Give a bounding box for every leukocyte visible.
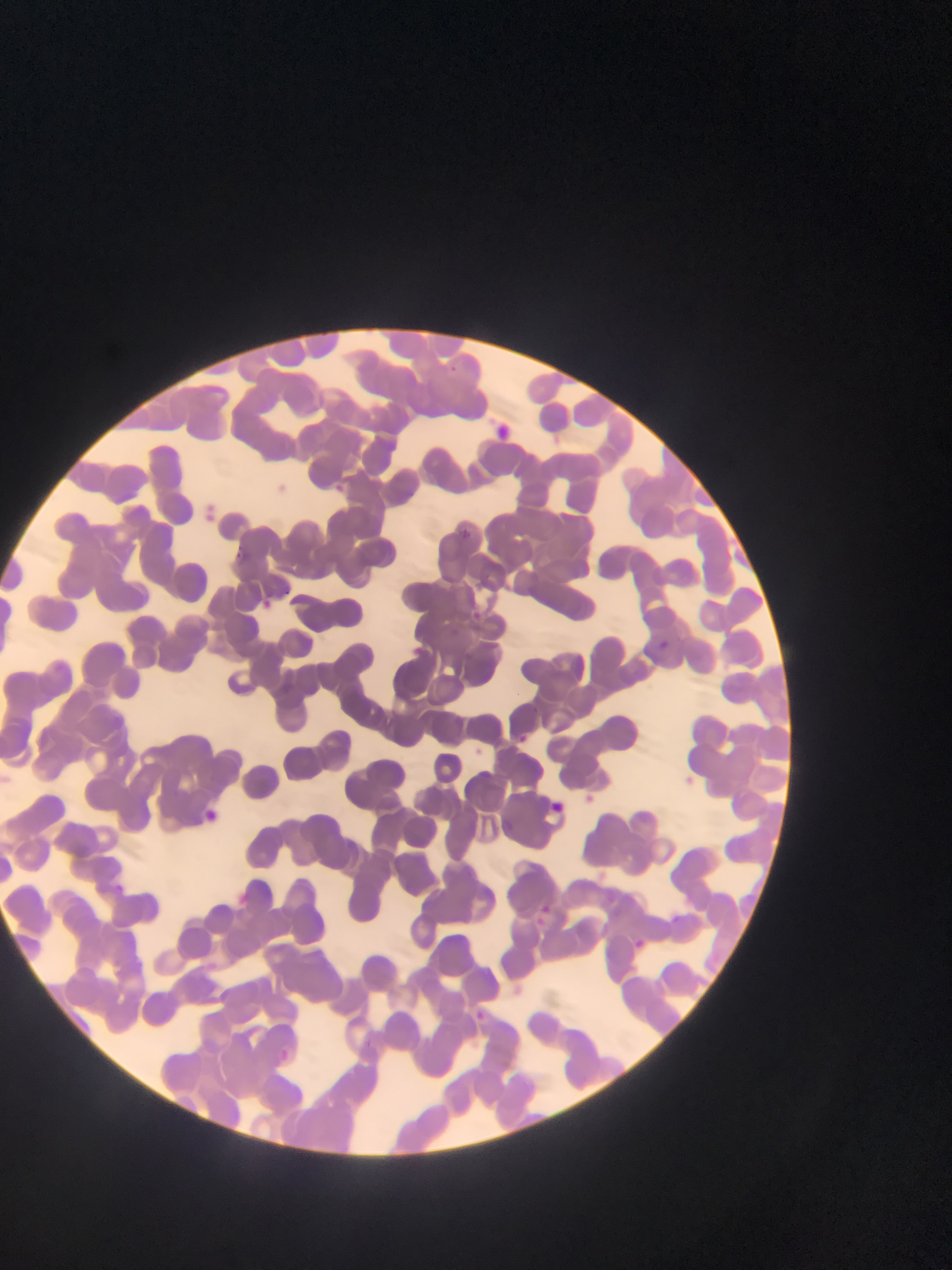
No leukocytes observed.

Approximate bounding boxes as (left, top, right, bottom) in pixels. Plasmodium parasite locations: (325, 480, 349, 501), (254, 595, 277, 616), (658, 632, 671, 660), (554, 793, 577, 817), (203, 805, 217, 828), (226, 888, 256, 913), (628, 934, 652, 956), (470, 1005, 493, 1026), (271, 1046, 296, 1068). Image is 952×1270 pixels. Photographed through a microscope with a mobile-phone camera. Single field of view. Collected in Ghana. Thin blood smear.